Comment on the morphology of the red blood cells.
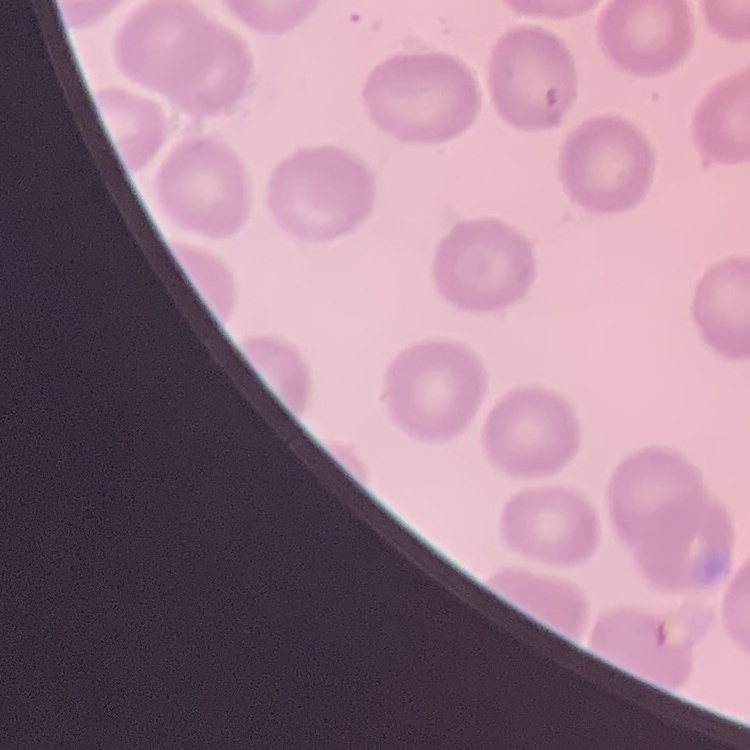
They show no rouleaux formation.

image type = square crop of a larger photomicrograph
stain = Field's or Giemsa
preparation = thin blood smear